Give the position of every malaria parasite.
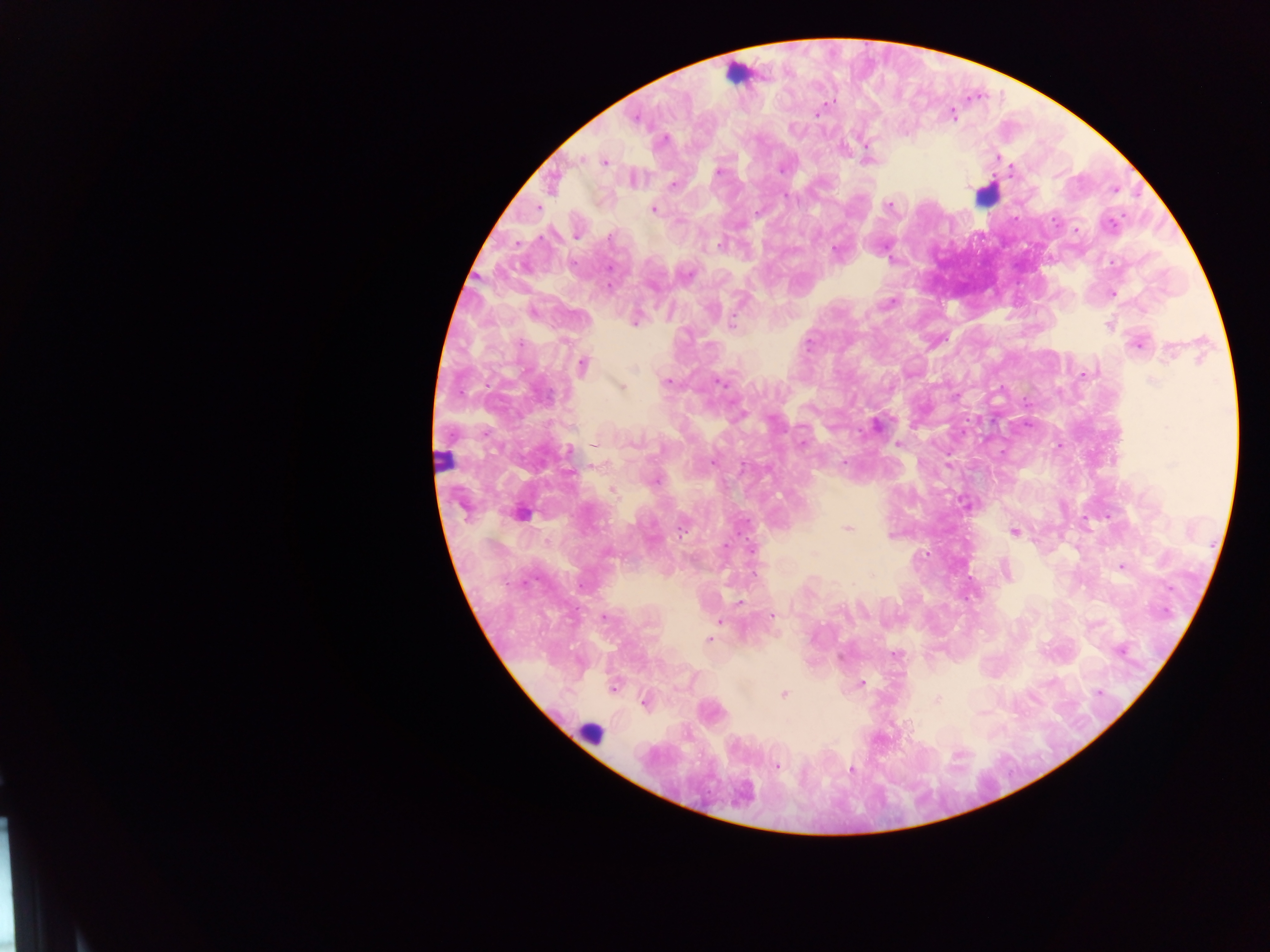
Approximate centers as [x, y] in pixels.
Malaria parasites: [832, 99], [819, 115], [796, 128], [995, 156], [868, 158], [604, 162], [781, 169], [1013, 170], [718, 171], [669, 185], [889, 204], [654, 211], [681, 218], [1076, 230], [720, 244], [838, 251], [1110, 262], [609, 285], [1114, 293], [891, 302], [635, 323], [1110, 325], [733, 326], [1135, 344], [1169, 349], [583, 366], [737, 367], [636, 368], [1081, 375], [1152, 379], [666, 382], [719, 382], [621, 386], [876, 424], [636, 439], [899, 443], [593, 445], [1055, 445], [569, 450], [843, 464], [741, 467], [655, 481], [613, 490], [965, 504], [848, 529], [683, 530], [1013, 531], [606, 550], [813, 553], [1121, 567], [1004, 569], [666, 574], [740, 601], [603, 615], [772, 616], [717, 621], [707, 640], [861, 684], [614, 688], [783, 694], [1099, 696], [935, 701], [643, 705], [907, 728], [778, 766], [850, 769].

field of view = single
image size = 1270×952 pixels
leukocyte locations = approximate centers as [x, y] in pixels: [736, 75], [981, 197], [442, 461], [590, 738]
country = Ghana
capture = mobile-phone photograph through a microscope
preparation = thick blood smear